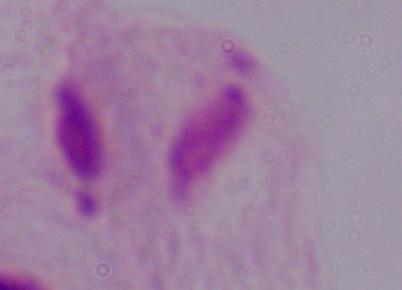
magnification = 1000x
modality = micrograph
identification = trichomonad